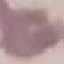
Malaria status: uninfected. Photographed with a smartphone camera at the microscope eyepiece. Thin smear of blood. Automatically extracted cell patch, resized to 64 × 64 pixels. Giemsa stain.